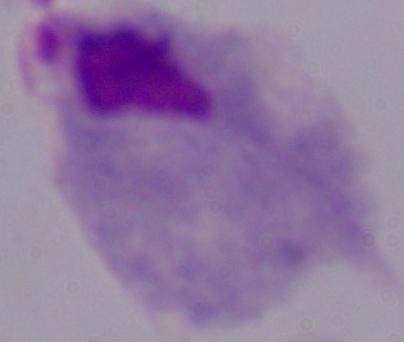

Summary:
  - Modality: photomicrograph
  - Identification: trichomonad
  - Magnification: 1000x